State which cell type is depicted.
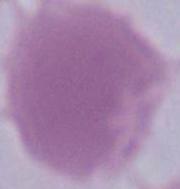

An erythrocyte.

modality = photomicrograph
magnification = 1000x